Name the parasite shown.
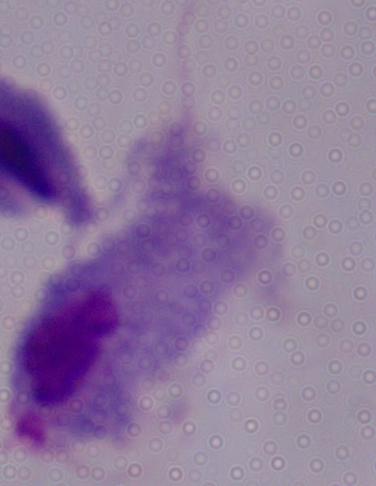
This is a trichomonad.

Photomicrograph. Captured at 1000x magnification.